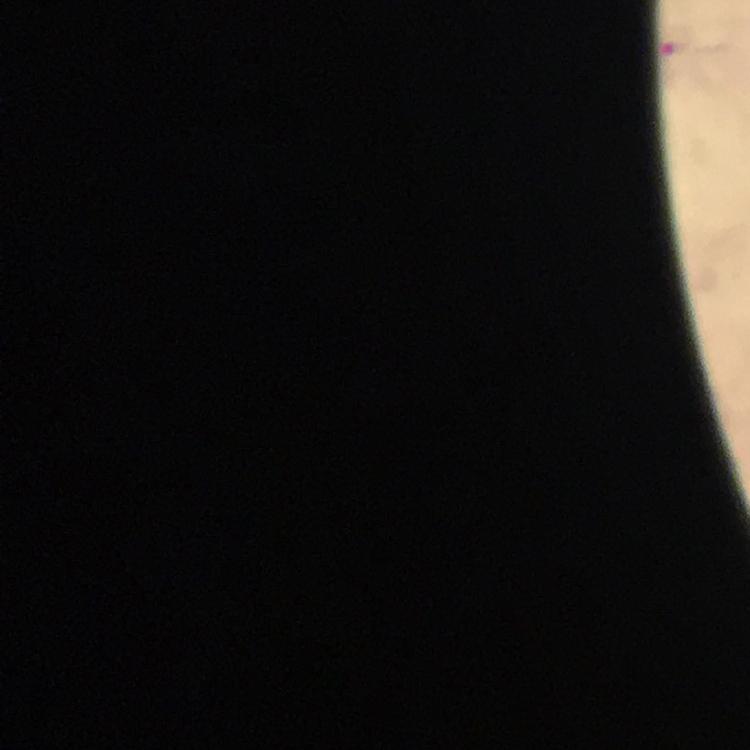

Approximate centers as {x, y} in pixels.
Summary:
  - Malaria parasite locations: {679, 47}
  - Preparation: thick blood film
  - Stain: Giemsa
  - Immersion oil: used
  - Magnification: 100x
  - Image size: 750×750 pixels
  - Cropped from: a single field of view
  - Context: from a diagnostic examination for malaria
  - Capture: smartphone camera through the microscope